Classify this cell by malaria status.
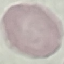

Uninfected.

Acquired by smartphone through the microscope eyepiece. Cell patch, automatically extracted from a larger field of view and resized to 64 × 64 pixels. Giemsa stain. Thin smear of blood.